Look for Plasmodium parasites.
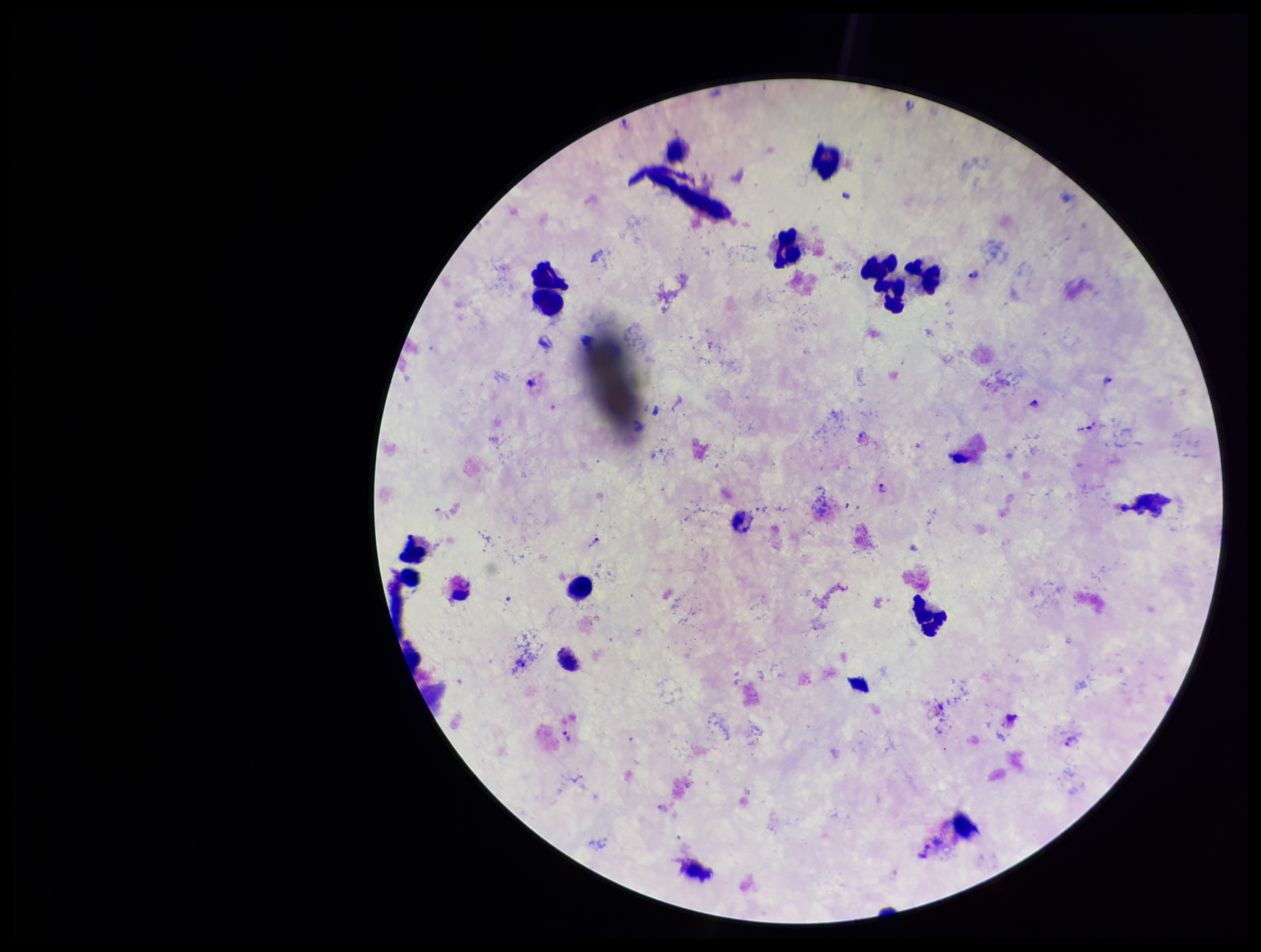
Detected.

patient_malaria_status: infected
image_size: 1261×952 pixels
stain: Giemsa
field_of_view: one from this slide
parasite_count: 6
preparation: thick blood smear
species_reported_for_this_patient: Plasmodium vivax
leukocyte_count: 11
capture: smartphone photograph through the microscope eyepiece